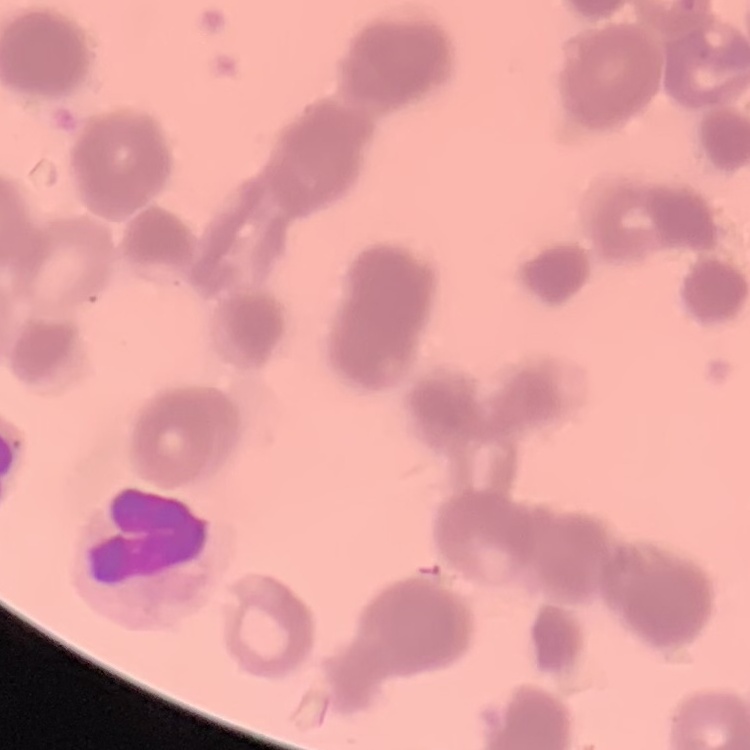

Summary:
  - Erythrocyte morphology: rouleaux formation
  - Stain: Field's or Giemsa
  - Image type: square crop of a larger photomicrograph
  - Preparation: thin blood film